Assess this cell for malaria.
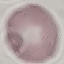
Uninfected.

{
  "preparation": "thin blood smear",
  "image_type": "cell patch, automatically extracted from a larger field of view and resized to 64 × 64 pixels",
  "stain": "Giemsa",
  "capture": "smartphone through the microscope eyepiece"
}